Name the blood parasite species.
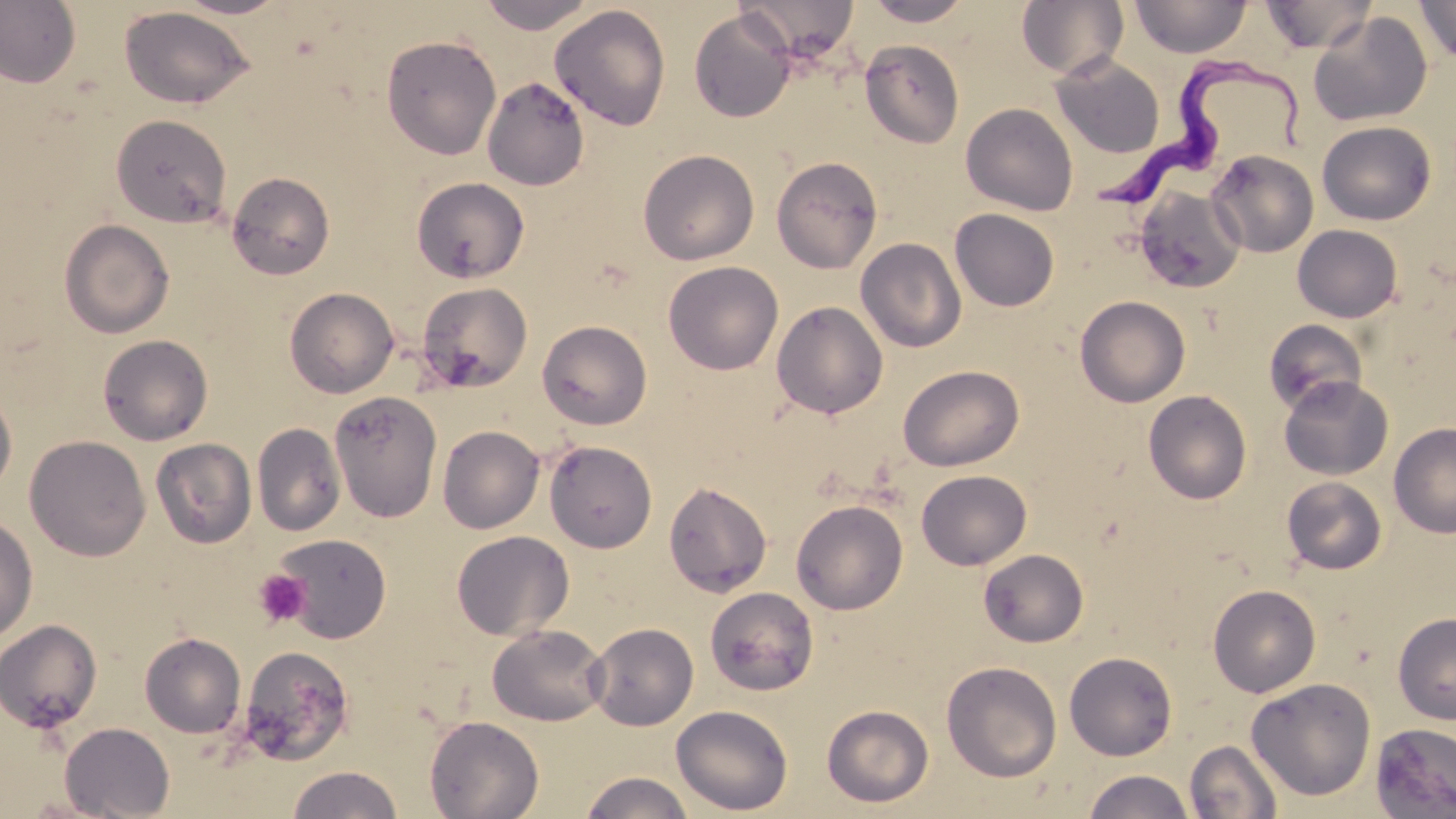
Trypanosoma brucei.

Approximate bounding boxes as named x1/y1/x2/y2 corners in pixels. Platelet locations: (x1=254, y1=569, x2=311, y2=627). Trypanosoma brucei locations: (x1=1087, y1=53, x2=1308, y2=211). Uninfected red blood cell locations: (x1=0, y1=0, x2=81, y2=88), (x1=172, y1=0, x2=291, y2=18), (x1=476, y1=0, x2=601, y2=33), (x1=738, y1=0, x2=860, y2=60), (x1=862, y1=0, x2=974, y2=26), (x1=1016, y1=0, x2=1128, y2=80), (x1=1017, y1=0, x2=1250, y2=72), (x1=1131, y1=0, x2=1251, y2=58), (x1=1260, y1=0, x2=1377, y2=54), (x1=1416, y1=0, x2=1456, y2=65), (x1=550, y1=4, x2=671, y2=131), (x1=119, y1=6, x2=255, y2=109), (x1=689, y1=9, x2=796, y2=123), (x1=1307, y1=11, x2=1433, y2=127), (x1=381, y1=34, x2=502, y2=161), (x1=860, y1=39, x2=965, y2=148), (x1=1050, y1=55, x2=1165, y2=158), (x1=482, y1=76, x2=590, y2=191), (x1=960, y1=103, x2=1078, y2=216), (x1=111, y1=113, x2=232, y2=227), (x1=1307, y1=121, x2=1415, y2=321), (x1=1317, y1=121, x2=1436, y2=225), (x1=637, y1=149, x2=759, y2=266), (x1=1207, y1=149, x2=1318, y2=257), (x1=771, y1=155, x2=882, y2=274), (x1=227, y1=171, x2=335, y2=280), (x1=411, y1=176, x2=529, y2=283), (x1=1134, y1=187, x2=1246, y2=294), (x1=949, y1=208, x2=1060, y2=311), (x1=59, y1=219, x2=174, y2=339), (x1=1292, y1=224, x2=1403, y2=322), (x1=855, y1=237, x2=967, y2=353), (x1=663, y1=261, x2=784, y2=375), (x1=417, y1=282, x2=532, y2=393), (x1=284, y1=287, x2=399, y2=398), (x1=1075, y1=296, x2=1191, y2=407), (x1=771, y1=301, x2=888, y2=419), (x1=1263, y1=319, x2=1368, y2=415), (x1=537, y1=320, x2=652, y2=430), (x1=97, y1=334, x2=213, y2=446), (x1=898, y1=365, x2=1024, y2=471), (x1=1278, y1=376, x2=1393, y2=480), (x1=0, y1=383, x2=17, y2=499), (x1=328, y1=390, x2=443, y2=522), (x1=1143, y1=390, x2=1252, y2=504), (x1=252, y1=423, x2=346, y2=536), (x1=1389, y1=423, x2=1456, y2=538), (x1=438, y1=425, x2=544, y2=533), (x1=24, y1=435, x2=150, y2=561), (x1=150, y1=438, x2=257, y2=548), (x1=544, y1=440, x2=657, y2=553), (x1=916, y1=469, x2=1032, y2=570), (x1=1282, y1=476, x2=1387, y2=574), (x1=663, y1=480, x2=772, y2=597), (x1=791, y1=499, x2=908, y2=615), (x1=0, y1=513, x2=38, y2=644), (x1=451, y1=530, x2=574, y2=641), (x1=270, y1=533, x2=392, y2=642), (x1=978, y1=548, x2=1089, y2=647), (x1=1208, y1=584, x2=1321, y2=697), (x1=704, y1=586, x2=819, y2=696), (x1=1393, y1=613, x2=1456, y2=724), (x1=0, y1=619, x2=103, y2=733), (x1=587, y1=622, x2=698, y2=730), (x1=487, y1=623, x2=610, y2=726), (x1=139, y1=632, x2=246, y2=738), (x1=236, y1=645, x2=356, y2=768), (x1=1064, y1=651, x2=1177, y2=760), (x1=942, y1=660, x2=1062, y2=782), (x1=1246, y1=678, x2=1376, y2=800), (x1=670, y1=704, x2=793, y2=816), (x1=822, y1=704, x2=934, y2=808), (x1=424, y1=715, x2=544, y2=819), (x1=59, y1=722, x2=175, y2=818), (x1=1371, y1=723, x2=1456, y2=818), (x1=1184, y1=740, x2=1283, y2=818), (x1=286, y1=765, x2=404, y2=818), (x1=1081, y1=769, x2=1197, y2=819), (x1=579, y1=771, x2=695, y2=819), (x1=16, y1=794, x2=125, y2=818). 1000x magnification. Single field of view. Thin blood film. Image is 1456×819 pixels. Light microscopy. May-Grünwald-Giemsa-stained preparation.